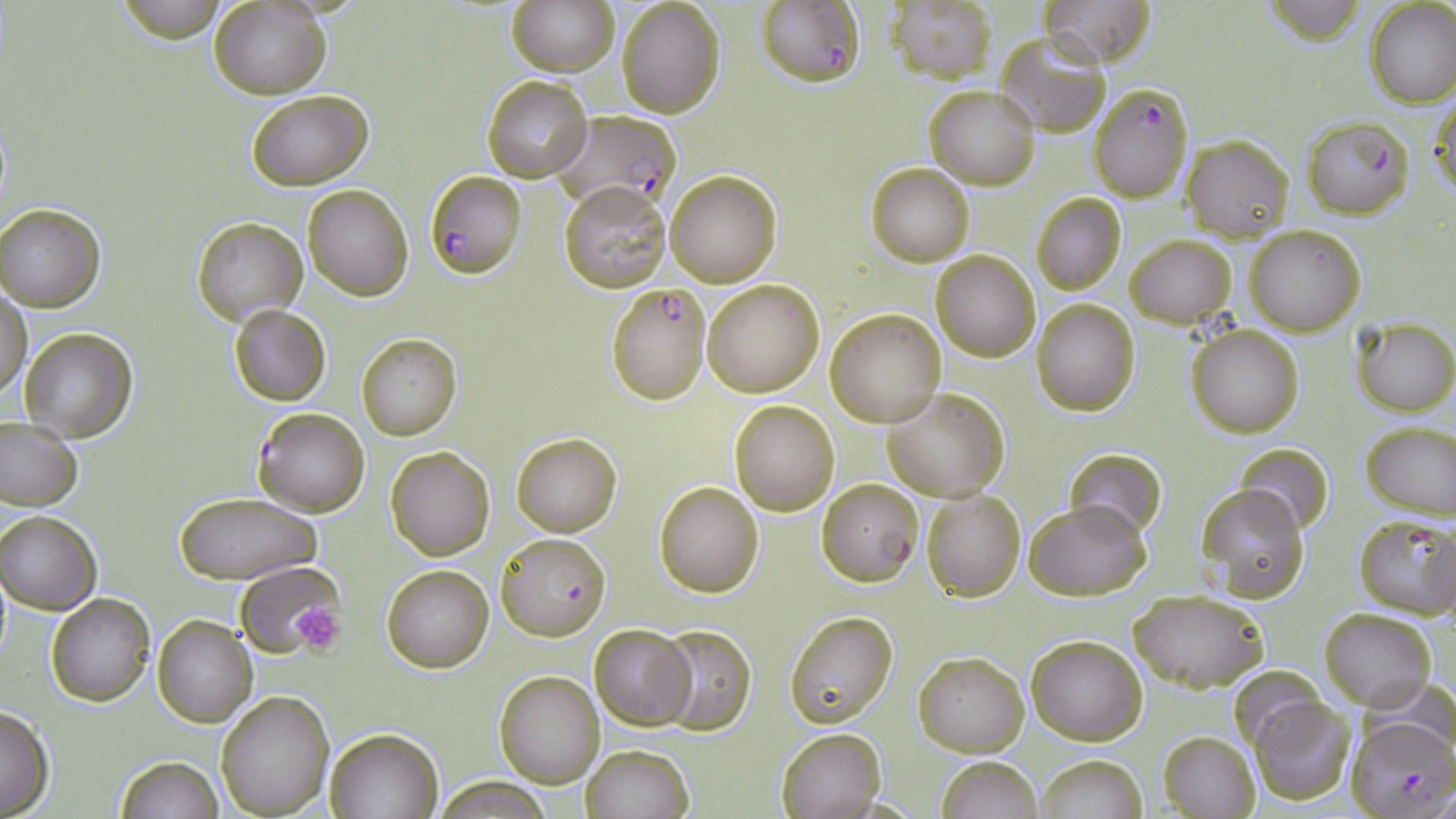

Summary:
  - Coordinate format: approximate bounding boxes as named x1/y1/x2/y2 corners in pixels
  - Uninfected red blood cell locations (subset): (x1=111, y1=0, x2=233, y2=39), (x1=507, y1=0, x2=618, y2=76), (x1=1042, y1=0, x2=1158, y2=66), (x1=1264, y1=0, x2=1365, y2=46), (x1=616, y1=1, x2=726, y2=118), (x1=884, y1=1, x2=996, y2=83), (x1=1366, y1=1, x2=1456, y2=107), (x1=210, y1=2, x2=328, y2=98), (x1=995, y1=35, x2=1111, y2=137), (x1=481, y1=75, x2=592, y2=182), (x1=925, y1=85, x2=1039, y2=189), (x1=246, y1=90, x2=372, y2=189), (x1=1431, y1=92, x2=1455, y2=204), (x1=1181, y1=134, x2=1294, y2=240), (x1=864, y1=163, x2=975, y2=266), (x1=664, y1=169, x2=782, y2=287), (x1=559, y1=181, x2=670, y2=294), (x1=303, y1=183, x2=414, y2=300), (x1=1030, y1=192, x2=1125, y2=295), (x1=1, y1=203, x2=105, y2=311), (x1=190, y1=217, x2=307, y2=324), (x1=1245, y1=224, x2=1366, y2=335), (x1=1126, y1=234, x2=1236, y2=327), (x1=932, y1=250, x2=1040, y2=362), (x1=701, y1=280, x2=825, y2=396), (x1=1, y1=288, x2=32, y2=401), (x1=1031, y1=299, x2=1141, y2=417), (x1=229, y1=304, x2=331, y2=405), (x1=825, y1=310, x2=945, y2=427), (x1=1350, y1=317, x2=1456, y2=417), (x1=1186, y1=323, x2=1305, y2=439), (x1=19, y1=328, x2=138, y2=443), (x1=355, y1=333, x2=462, y2=441), (x1=882, y1=387, x2=1011, y2=501), (x1=729, y1=400, x2=840, y2=515), (x1=0, y1=417, x2=83, y2=511), (x1=1359, y1=421, x2=1456, y2=519), (x1=511, y1=432, x2=621, y2=536), (x1=1235, y1=442, x2=1335, y2=534), (x1=386, y1=446, x2=495, y2=560), (x1=1064, y1=447, x2=1167, y2=538), (x1=655, y1=481, x2=764, y2=597), (x1=1197, y1=484, x2=1310, y2=602), (x1=920, y1=489, x2=1028, y2=602), (x1=173, y1=493, x2=322, y2=585), (x1=1024, y1=500, x2=1151, y2=601), (x1=1, y1=509, x2=101, y2=614), (x1=1352, y1=514, x2=1456, y2=620), (x1=236, y1=561, x2=344, y2=658), (x1=382, y1=565, x2=492, y2=673), (x1=1128, y1=588, x2=1270, y2=692), (x1=46, y1=594, x2=156, y2=707), (x1=1319, y1=608, x2=1437, y2=711), (x1=784, y1=610, x2=899, y2=727), (x1=153, y1=615, x2=257, y2=727), (x1=590, y1=624, x2=695, y2=730), (x1=654, y1=624, x2=754, y2=735), (x1=1026, y1=635, x2=1147, y2=745), (x1=913, y1=651, x2=1028, y2=757), (x1=1228, y1=664, x2=1329, y2=754), (x1=495, y1=671, x2=604, y2=788), (x1=216, y1=691, x2=335, y2=819), (x1=1250, y1=697, x2=1357, y2=805), (x1=0, y1=704, x2=56, y2=817), (x1=775, y1=727, x2=886, y2=819), (x1=325, y1=728, x2=442, y2=818), (x1=1157, y1=729, x2=1261, y2=819), (x1=580, y1=744, x2=694, y2=819), (x1=113, y1=754, x2=224, y2=819), (x1=1034, y1=755, x2=1148, y2=819), (x1=935, y1=757, x2=1043, y2=818), (x1=434, y1=775, x2=556, y2=818)
  - Platelet locations: (x1=289, y1=600, x2=346, y2=652)
  - Plasmodium falciparum-infected red blood cell locations (subset): (x1=755, y1=0, x2=864, y2=88), (x1=1090, y1=84, x2=1193, y2=202), (x1=549, y1=110, x2=684, y2=216), (x1=1302, y1=115, x2=1413, y2=220), (x1=606, y1=281, x2=711, y2=404), (x1=252, y1=407, x2=370, y2=516), (x1=817, y1=478, x2=922, y2=586), (x1=497, y1=531, x2=610, y2=640)
  - Slide-level diagnosis: Plasmodium falciparum
  - Preparation: thin blood smear
  - Modality: optical microscopy
  - Stain: May-Grünwald-Giemsa
  - Magnification: 1000x
  - Field of view: one of a larger specimen
  - Image size: 1456×819 pixels